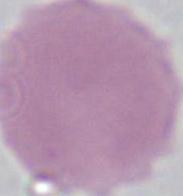
modality = photomicrograph
identification = erythrocyte
magnification = 1000x